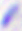
Summary:
  - Identification: Toxoplasma gondii
  - Modality: micrograph
  - Magnification: 400x